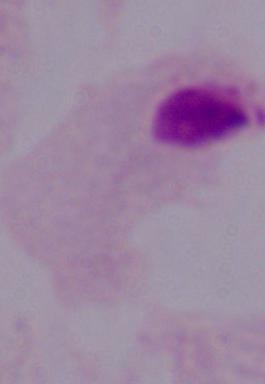
magnification: 1000x
modality: photomicrograph
identification: trichomonad